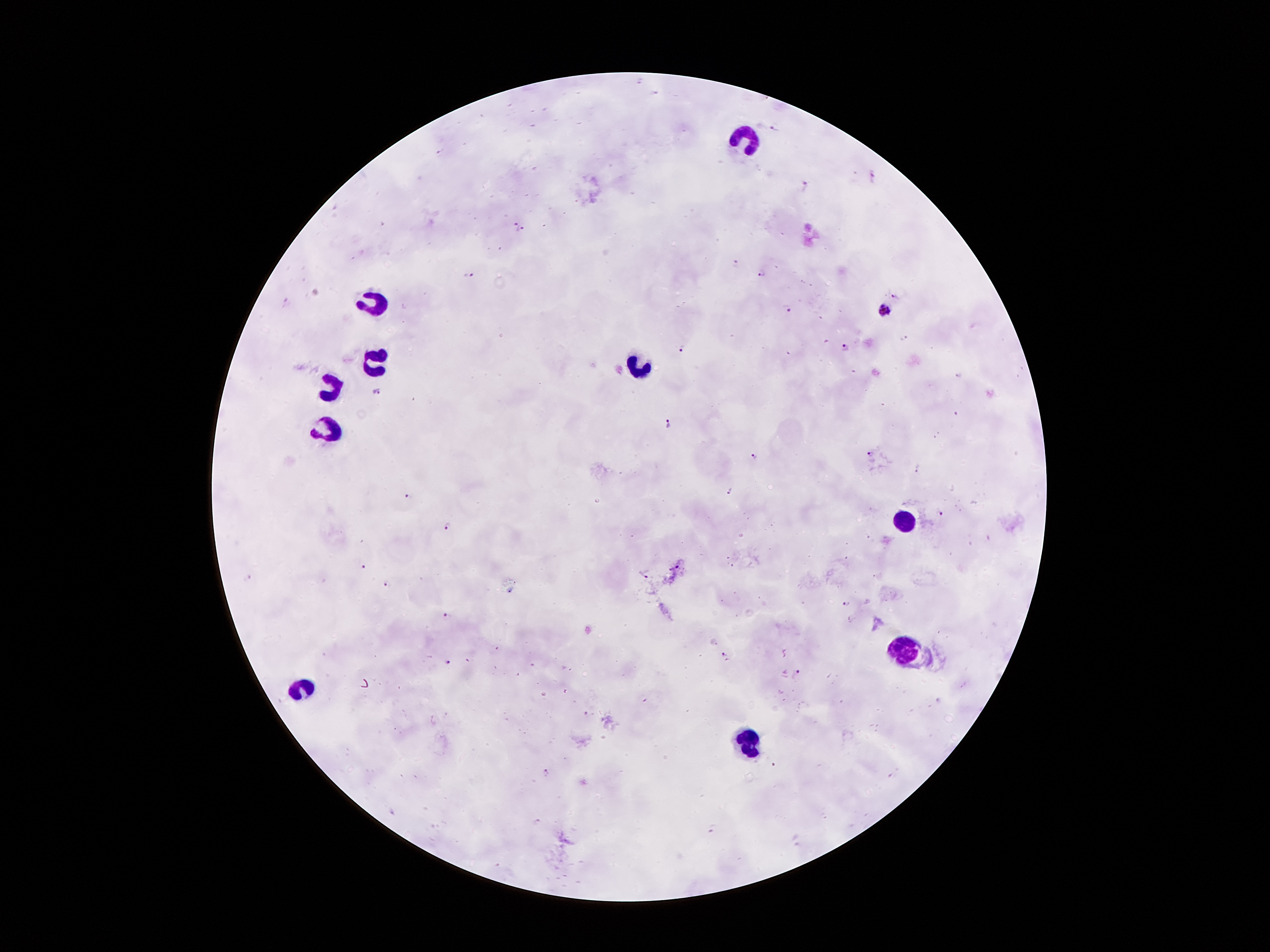
malaria_parasite_locations: 'approximate object centers, in pixels from the top-left corner: (x=774, y=128), (x=873, y=176), (x=807, y=186), (x=520, y=225), (x=737, y=264), (x=761, y=272), (x=469, y=275), (x=897, y=295), (x=288, y=300), (x=786, y=308), (x=887, y=312), (x=904, y=337), (x=846, y=347), (x=682, y=349), (x=377, y=390), (x=668, y=425), (x=871, y=454), (x=753, y=456), (x=918, y=468), (x=730, y=491), (x=408, y=496), (x=939, y=512), (x=448, y=526), (x=363, y=567), (x=646, y=573), (x=249, y=579), (x=388, y=585), (x=846, y=603), (x=446, y=615), (x=726, y=655), (x=447, y=661), (x=797, y=672), (x=773, y=765), (x=546, y=773), (x=537, y=822), (x=711, y=829)'
leukocyte_locations: 'approximate object centers, in pixels from the top-left corner: (x=746, y=138), (x=375, y=300), (x=375, y=363), (x=642, y=370), (x=335, y=389), (x=328, y=432), (x=903, y=519), (x=903, y=649), (x=302, y=687), (x=750, y=739)'
stain: Giemsa
field_of_view: one from this slide
patient_malaria_status: infected with Plasmodium falciparum
preparation: thick blood film
image_size: 1270×952 pixels
capture: smartphone through the microscope eyepiece
magnification: 100x